Report the malaria status of this cell.
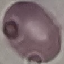

Uninfected.

Automatically extracted cell patch, resized to 64 × 64 pixels. Giemsa stain. Thin smear of blood. Photographed with a smartphone camera at the microscope eyepiece.